Classify this cell by malaria status.
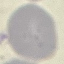
Uninfected.

Thin smear of blood. Acquired by smartphone through the microscope eyepiece. Giemsa stain. Automatically extracted cell patch, resized to 64 × 64 pixels.